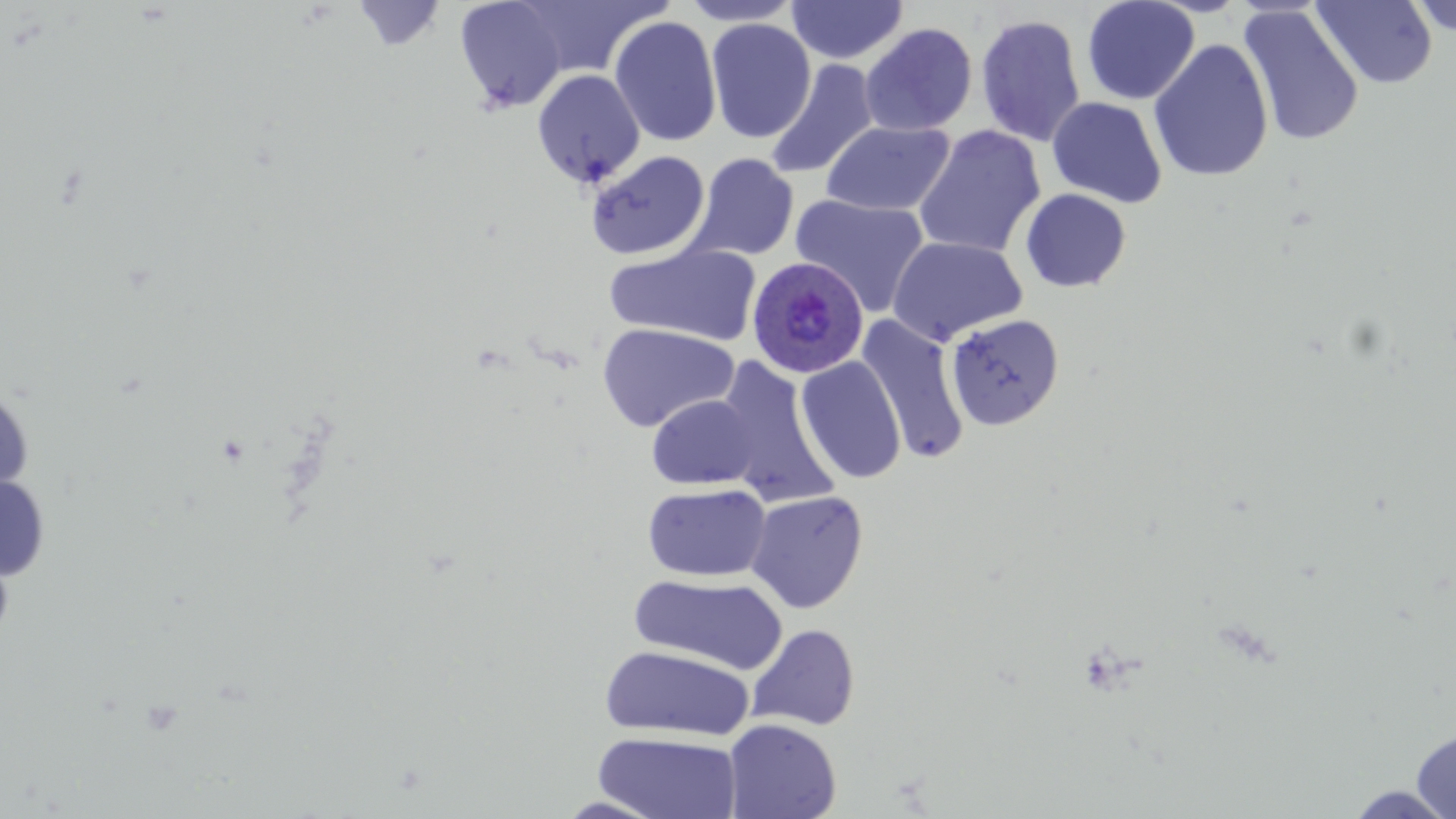
slide-level diagnosis = Plasmodium ovale
modality = light microscopy
field of view = single
uninfected red blood cell locations = approximate bounding boxes as [x1, y1, x2, y2] in pixels: [505, 0, 670, 83], [678, 0, 804, 26], [786, 0, 909, 65], [1082, 0, 1199, 105], [1406, 0, 1456, 38], [351, 1, 448, 53], [453, 1, 576, 113], [1311, 1, 1438, 89], [1238, 6, 1364, 147], [975, 13, 1087, 147], [608, 16, 722, 147], [705, 18, 816, 143], [859, 22, 978, 136], [1148, 39, 1274, 182], [766, 59, 880, 179], [532, 70, 646, 187], [1046, 97, 1167, 208], [821, 121, 956, 216], [912, 125, 1046, 259], [586, 150, 710, 260], [687, 153, 799, 261], [1020, 188, 1131, 293], [790, 194, 930, 317], [887, 235, 1028, 345], [604, 242, 762, 347], [857, 314, 970, 464], [945, 314, 1063, 431], [597, 323, 739, 432], [796, 356, 907, 484], [713, 358, 838, 506], [0, 382, 35, 503], [647, 395, 760, 490], [0, 472, 51, 583], [643, 482, 771, 582], [745, 490, 868, 612], [629, 573, 789, 674], [747, 623, 860, 732], [598, 645, 754, 741], [723, 718, 842, 819], [1412, 727, 1456, 819], [593, 731, 743, 818], [1341, 785, 1456, 819], [555, 796, 666, 818]
image size = 1456×819 pixels
preparation = thin blood film
stain = May-Grünwald-Giemsa
Plasmodium ovale-infected red blood cell locations = approximate bounding boxes as [x1, y1, x2, y2] in pixels: [746, 254, 870, 380]
magnification = 1000x